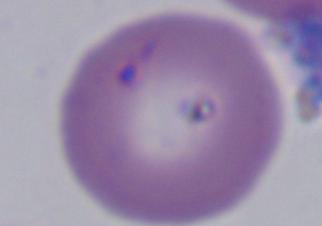

{
  "identification": "Babesia",
  "modality": "photomicrograph",
  "magnification": "1000x"
}